Point out each Plasmodium parasite.
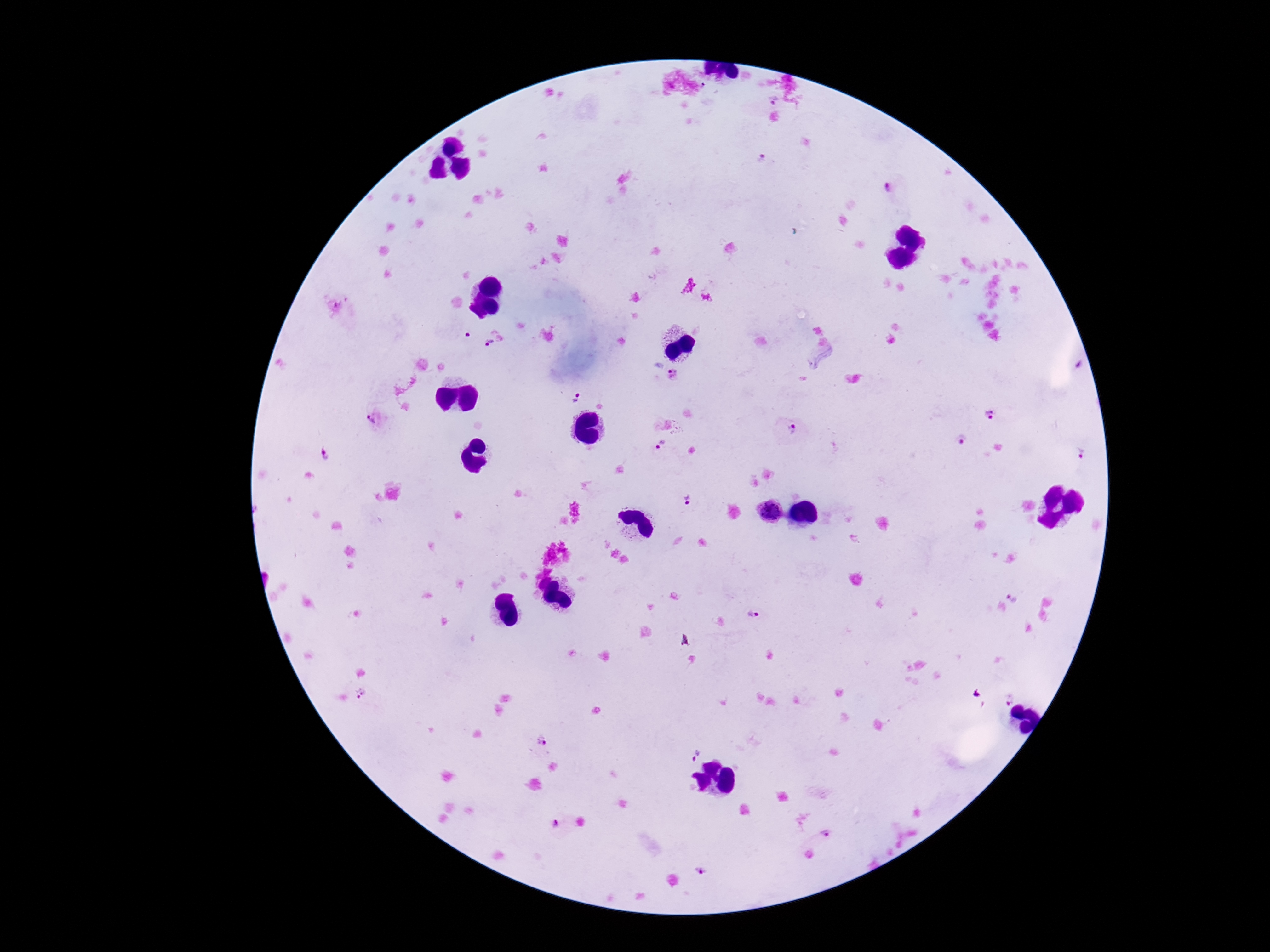

Approximate object centers, in pixels from the top-left corner.
Plasmodium parasites: (x=772, y=99), (x=763, y=159), (x=889, y=187), (x=494, y=337), (x=673, y=375), (x=575, y=396), (x=990, y=414), (x=375, y=417), (x=788, y=428), (x=960, y=440), (x=660, y=445), (x=1080, y=454), (x=325, y=456), (x=687, y=497), (x=1015, y=592), (x=754, y=614), (x=362, y=695), (x=1006, y=696), (x=541, y=741), (x=688, y=749), (x=555, y=825), (x=825, y=835), (x=705, y=871).

patient malaria status = positive
magnification = 100x
image size = 1270×952 pixels
capture = smartphone camera through the microscope eyepiece
preparation = thick blood smear
stain = Giemsa
field of view = single